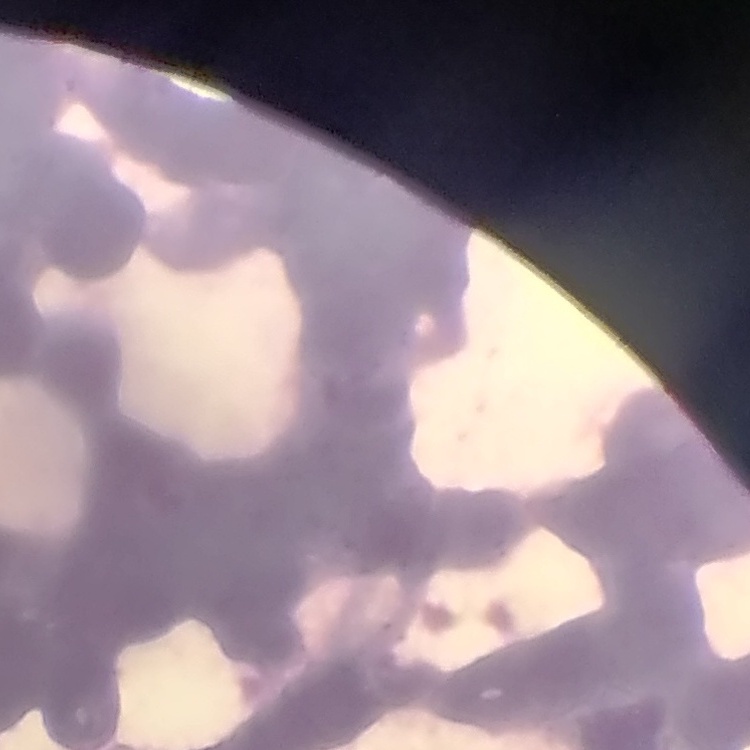

Summary:
  - Erythrocyte morphology: rouleaux formation
  - Preparation: thin blood film
  - Image type: one tile cut from a larger photomicrograph
  - Stain: Field's or Giemsa